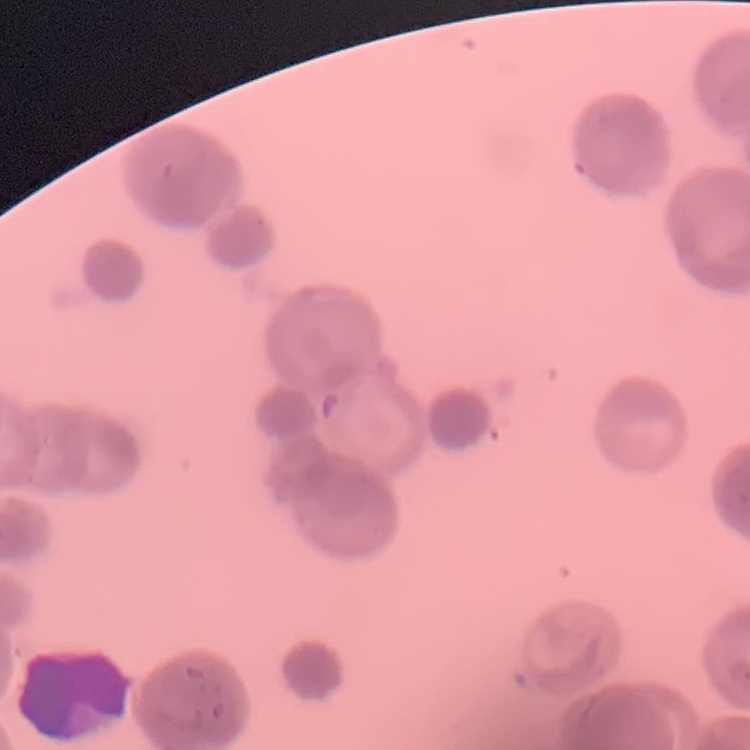

The erythrocytes exhibit rouleaux formation. Square crop of a larger photomicrograph. Field's or Giemsa stain. Thin peripheral smear.